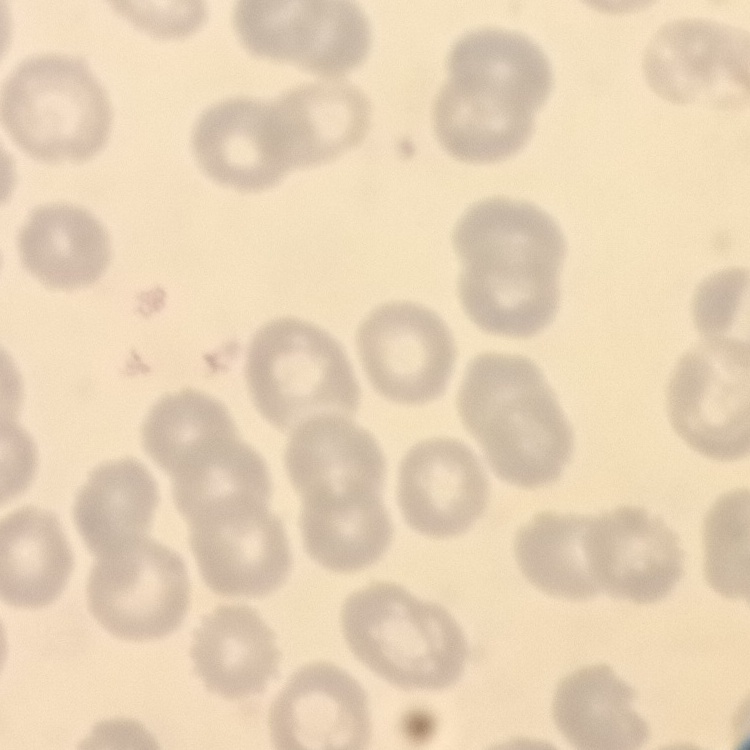

The red blood cells exhibit no rouleaux formation. Thin peripheral smear. Field's or Giemsa stain. One tile cut from a larger photomicrograph.